Assess this cell for malaria.
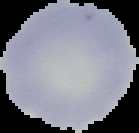

Uninfected.

The area outside the segmented cell region is set to black. Image is 139×133 pixels. From a thin blood smear.